Assess this cell for malaria.
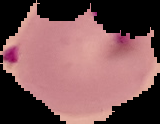

It is parasitized.

Image is 160×124 pixels. From a thin blood film. Segmented cell region on a black background.